Assess this cell for malaria.
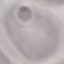

It is uninfected.

stain: Giemsa
image_type: cell patch, automatically extracted from a larger field of view and resized to 64 × 64 pixels
capture: smartphone camera at the microscope eyepiece
preparation: thin smear